Comment on the morphology of the red blood cells.
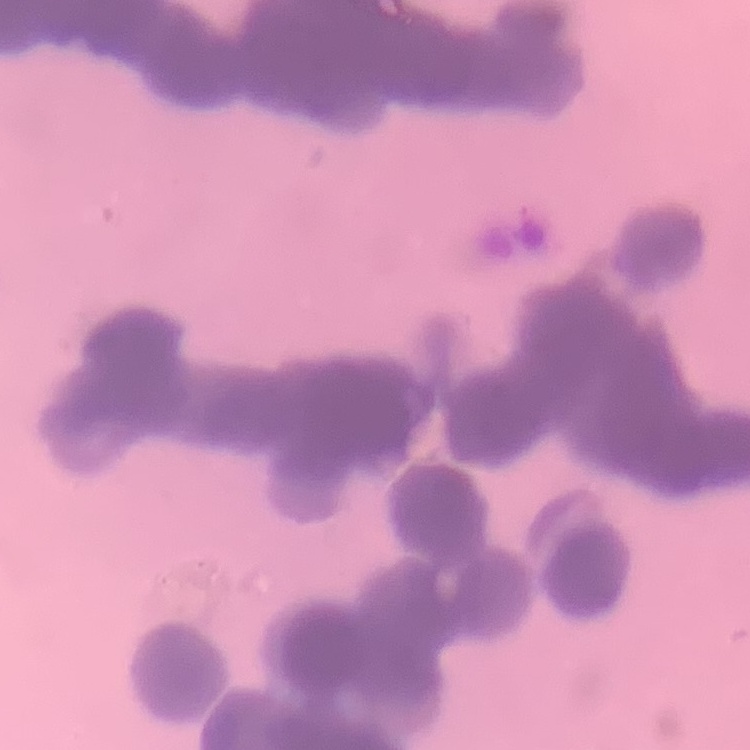

They show rouleaux formation.

Summary:
  - Stain: Field's or Giemsa
  - Preparation: thin blood film
  - Image type: one tile cut from a larger photomicrograph